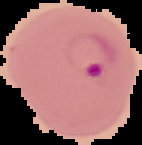

Image is 142×145 pixels. From a thin blood film. The area outside the segmented cell region is set to black. Result: Plasmodium parasites detected.